Report the malaria status of this cell.
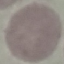

It is uninfected.

image type = automatically extracted cell patch, resized to 64 × 64 pixels
preparation = thin blood smear
stain = Giemsa
capture = smartphone through the microscope eyepiece